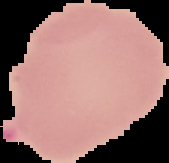
image size = 169×163 pixels
preparation = thin blood smear
result = no Plasmodium parasites detected
image type = cell region segmented out of the field of view; surrounding area masked to black